Mark where leukocytes are.
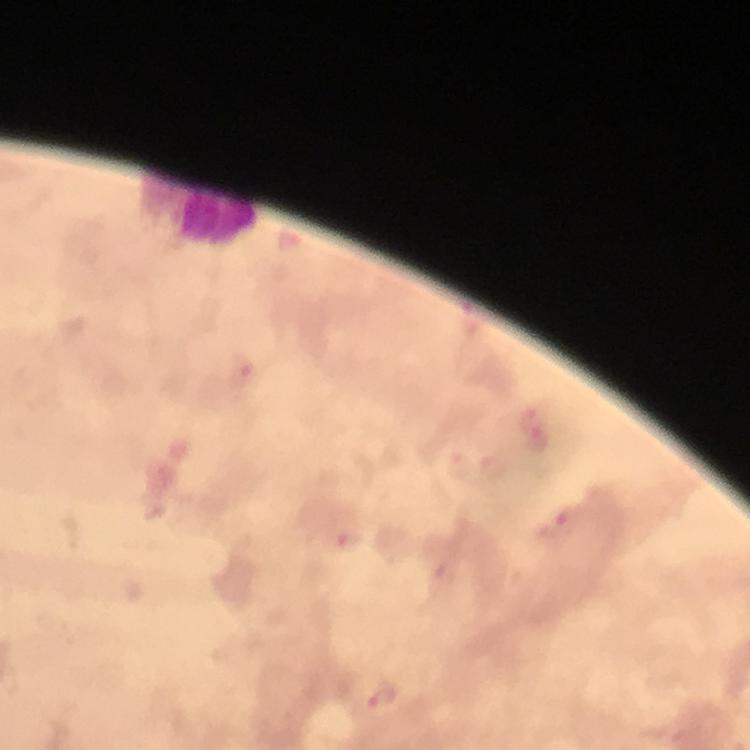
Approximate centers as [x, y] in pixels.
Leukocytes: [217, 222].

{
  "context": "from a malaria diagnostic workup",
  "preparation": "thick blood smear",
  "plasmodium_parasite_locations": "approximate centers as [x, y] in pixels: [241, 370], [534, 429], [559, 523], [349, 542], [381, 696]",
  "capture": "smartphone photograph through a microscope",
  "immersion_oil": "applied",
  "cropped_from": "a single field of view",
  "image_size": "750×750 pixels",
  "magnification": "100x",
  "stain": "Giemsa"
}